State which parasite is depicted.
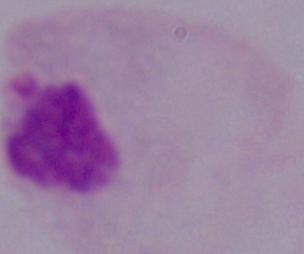

This is a trichomonad.

magnification = 1000x
modality = photomicrograph